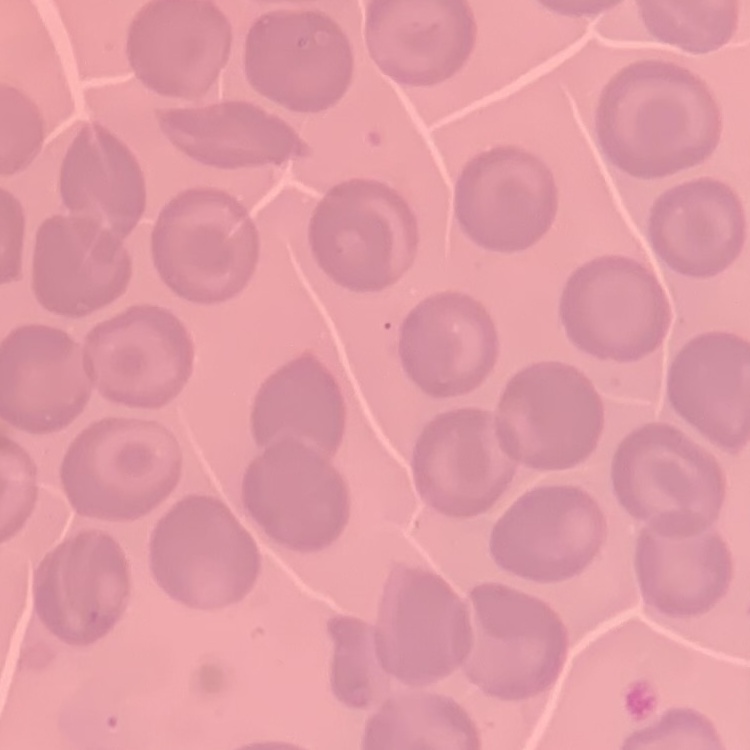
{
  "red_blood_cell_morphology": "no rouleaux formation",
  "image_type": "square crop of a larger photomicrograph",
  "preparation": "thin peripheral smear",
  "stain": "Field's or Giemsa"
}